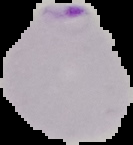

result = malaria parasites detected
image size = 133×145 pixels
image type = segmented cell region on a black background
preparation = thin blood smear